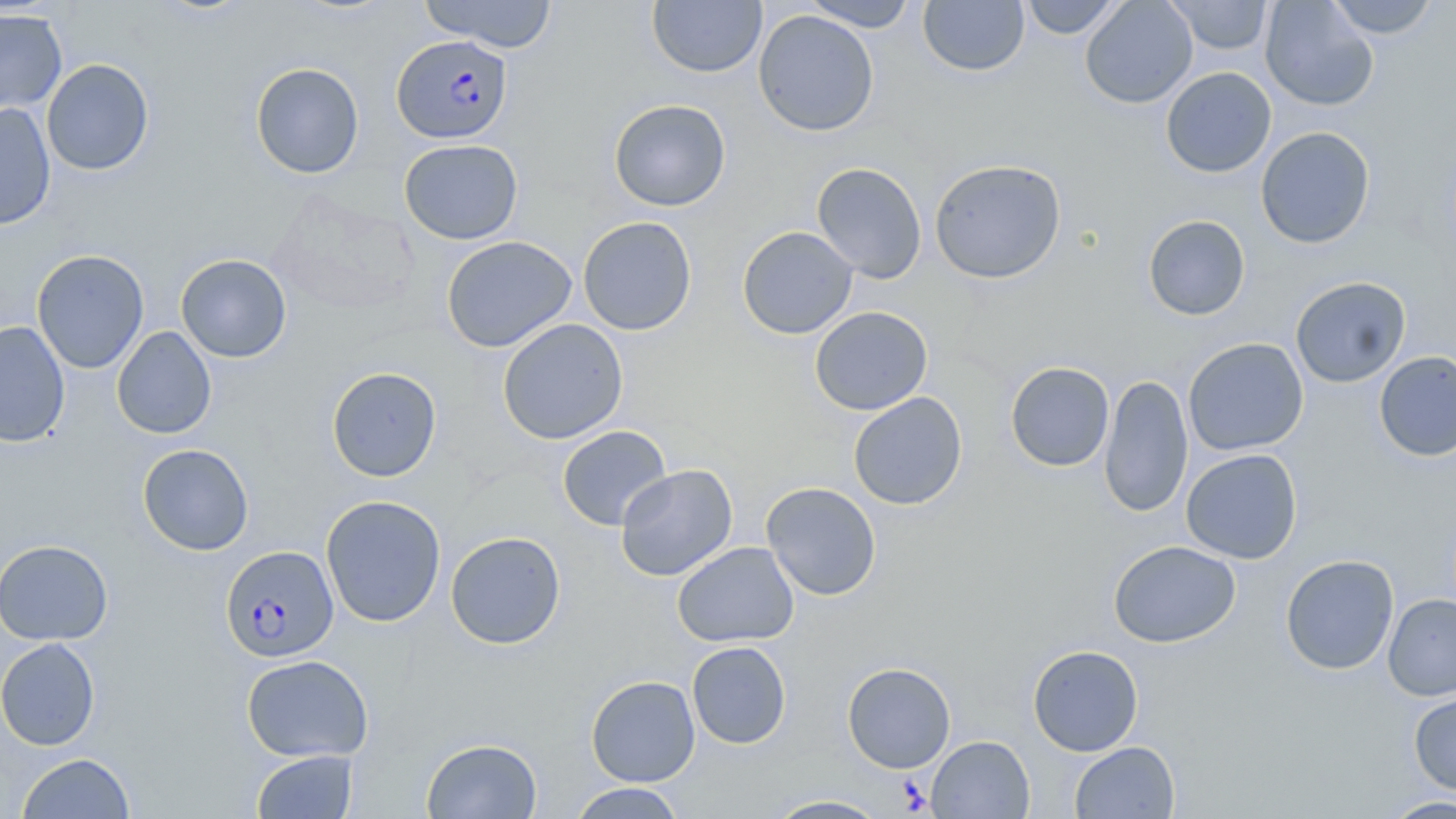
slide-level diagnosis = Plasmodium falciparum
modality = optical microscopy
magnification = 1000x
preparation = thin blood smear
image size = 1456×819 pixels
stain = May-Grünwald-Giemsa
uninfected red blood cell locations = approximate bounding boxes as [x1, y1, x2, y2] in pixels: [419, 0, 558, 52], [802, 0, 918, 31], [1019, 0, 1125, 39], [1080, 0, 1198, 108], [1167, 0, 1273, 55], [1260, 0, 1379, 111], [1325, 0, 1440, 39], [647, 1, 766, 78], [918, 1, 1030, 76], [0, 8, 68, 115], [753, 10, 879, 136], [7, 23, 99, 143], [41, 59, 155, 176], [250, 62, 364, 179], [1160, 67, 1277, 178], [608, 99, 731, 212], [0, 102, 56, 230], [1256, 126, 1375, 249], [399, 139, 523, 245], [929, 158, 1067, 284], [812, 162, 927, 283], [1143, 215, 1250, 321], [577, 216, 697, 335], [737, 226, 858, 339], [440, 236, 577, 353], [32, 249, 149, 373], [175, 254, 292, 362], [1290, 276, 1411, 388], [810, 306, 933, 415], [497, 318, 629, 444], [0, 321, 71, 448], [112, 326, 217, 439], [1183, 337, 1308, 456], [1374, 351, 1456, 462], [1005, 361, 1115, 472], [326, 366, 442, 482], [1099, 373, 1193, 518], [848, 392, 967, 510], [557, 425, 672, 531], [137, 444, 254, 556], [1181, 448, 1303, 564], [615, 464, 738, 581], [761, 482, 881, 600], [320, 495, 447, 627], [445, 531, 566, 649], [0, 539, 114, 645], [1108, 540, 1241, 648], [672, 541, 799, 647], [1280, 554, 1399, 675], [1383, 594, 1456, 700], [0, 637, 101, 750], [687, 641, 791, 749], [1027, 644, 1144, 756], [241, 654, 373, 762], [842, 662, 956, 772], [586, 675, 700, 787], [1409, 691, 1456, 796], [927, 735, 1034, 818], [421, 738, 542, 818], [1069, 741, 1179, 818], [252, 749, 358, 818], [17, 752, 136, 818], [567, 783, 687, 818], [762, 795, 891, 818], [1380, 795, 1456, 819]
field of view = single
Plasmodium falciparum-infected red blood cell locations = approximate bounding boxes as [x1, y1, x2, y2] in pixels: [391, 35, 512, 144], [221, 543, 341, 663]